Identify the blood parasite species.
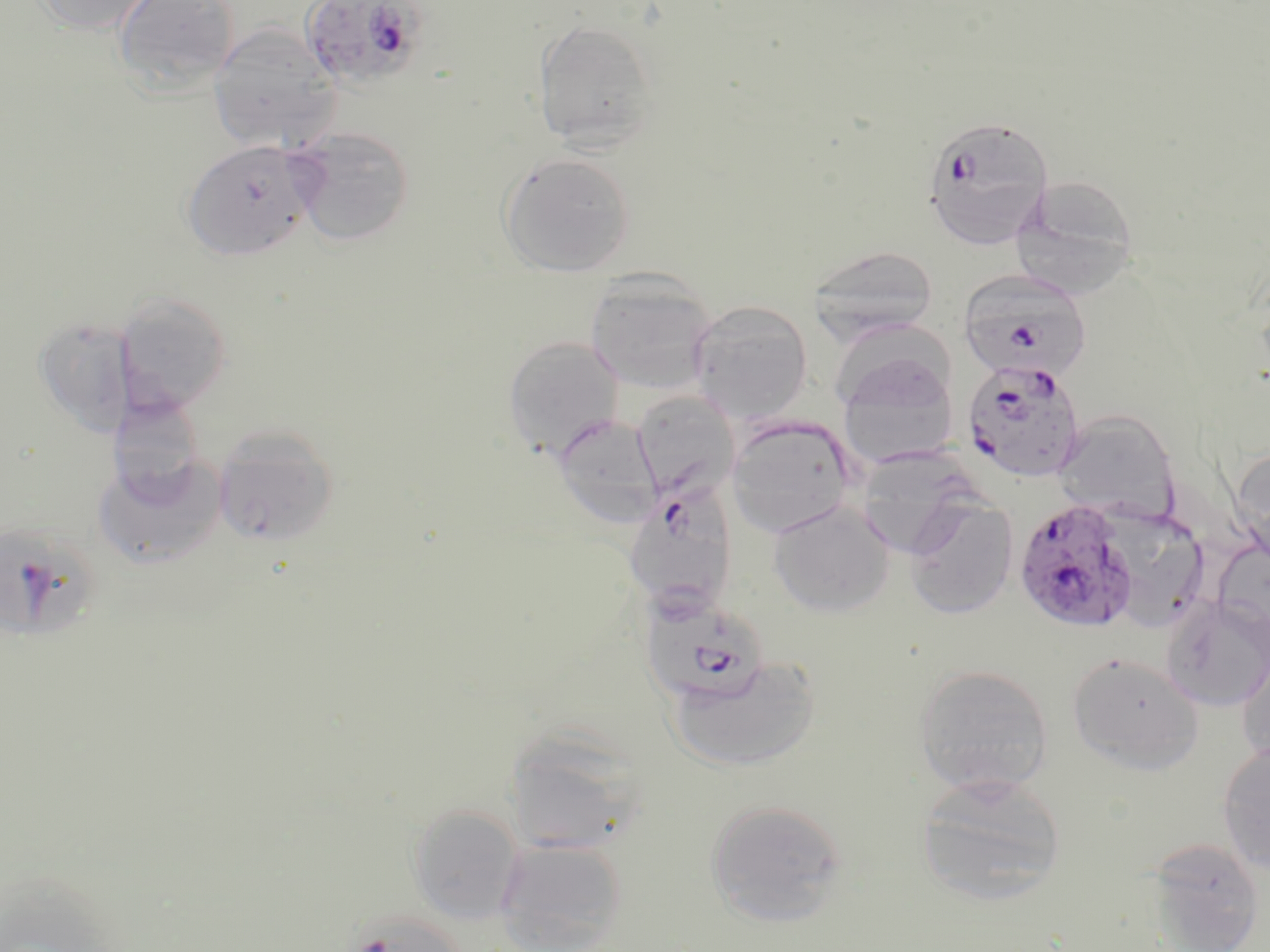
Plasmodium falciparum.

Approximate bounding boxes as named x1/y1/x2/y2 corners in pixels. Plasmodium falciparum-infected red blood cell locations: (x1=298, y1=0, x2=432, y2=90), (x1=921, y1=113, x2=1054, y2=250), (x1=958, y1=270, x2=1093, y2=384), (x1=961, y1=358, x2=1086, y2=483), (x1=622, y1=483, x2=738, y2=616), (x1=1013, y1=498, x2=1139, y2=633), (x1=639, y1=593, x2=780, y2=727). Uninfected red blood cell locations: (x1=33, y1=0, x2=157, y2=36), (x1=113, y1=0, x2=240, y2=96), (x1=532, y1=18, x2=660, y2=154), (x1=208, y1=24, x2=341, y2=153), (x1=288, y1=127, x2=416, y2=246), (x1=181, y1=139, x2=317, y2=262), (x1=497, y1=151, x2=637, y2=278), (x1=1010, y1=176, x2=1142, y2=298), (x1=808, y1=245, x2=938, y2=341), (x1=585, y1=271, x2=718, y2=395), (x1=114, y1=291, x2=233, y2=415), (x1=688, y1=300, x2=813, y2=422), (x1=833, y1=313, x2=957, y2=410), (x1=503, y1=335, x2=625, y2=460), (x1=836, y1=349, x2=961, y2=471), (x1=630, y1=388, x2=740, y2=507), (x1=107, y1=393, x2=205, y2=501), (x1=1053, y1=410, x2=1182, y2=525), (x1=552, y1=413, x2=663, y2=528), (x1=726, y1=415, x2=857, y2=538), (x1=213, y1=424, x2=340, y2=547), (x1=1232, y1=443, x2=1270, y2=566), (x1=854, y1=447, x2=981, y2=556), (x1=93, y1=453, x2=228, y2=568), (x1=904, y1=495, x2=1018, y2=619), (x1=768, y1=499, x2=896, y2=617), (x1=1095, y1=504, x2=1210, y2=630), (x1=0, y1=518, x2=103, y2=646), (x1=1161, y1=595, x2=1270, y2=711), (x1=1236, y1=639, x2=1270, y2=771), (x1=1066, y1=651, x2=1203, y2=773), (x1=665, y1=656, x2=822, y2=772), (x1=913, y1=663, x2=1053, y2=796), (x1=504, y1=728, x2=650, y2=855), (x1=1217, y1=742, x2=1270, y2=874), (x1=917, y1=773, x2=1066, y2=906), (x1=705, y1=798, x2=849, y2=925), (x1=407, y1=803, x2=525, y2=924), (x1=495, y1=836, x2=629, y2=952), (x1=1142, y1=836, x2=1267, y2=952). Thin blood smear. Image is 1270×952 pixels. Captured at 1000x magnification. Light microscopy. Single field of view. May-Grünwald-Giemsa stain.